Assess the morphology of the red blood cells.
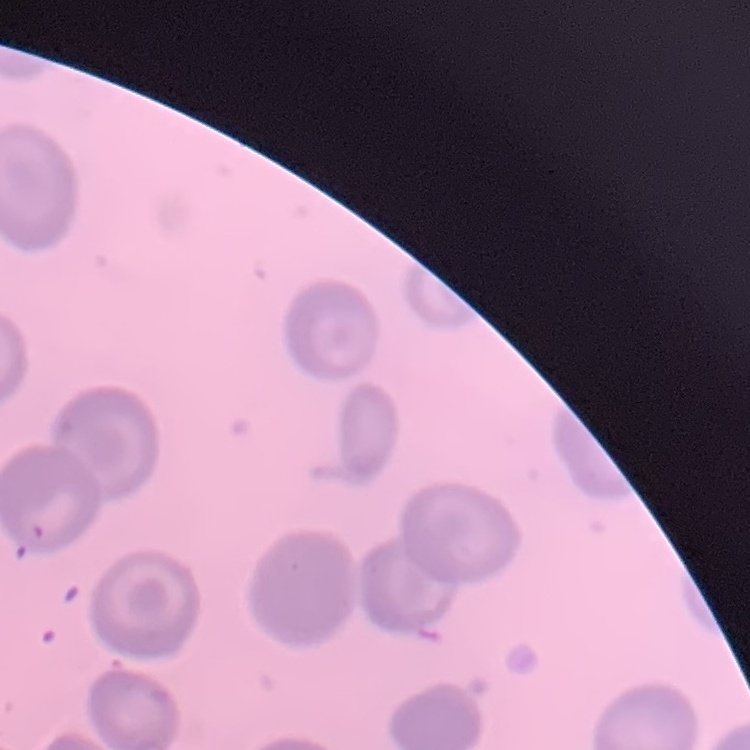
No rouleaux formation.

Summary:
  - Preparation: thin blood smear
  - Stain: Field's or Giemsa
  - Image type: square crop of a larger photomicrograph